Outline each blood parasite and name the species.
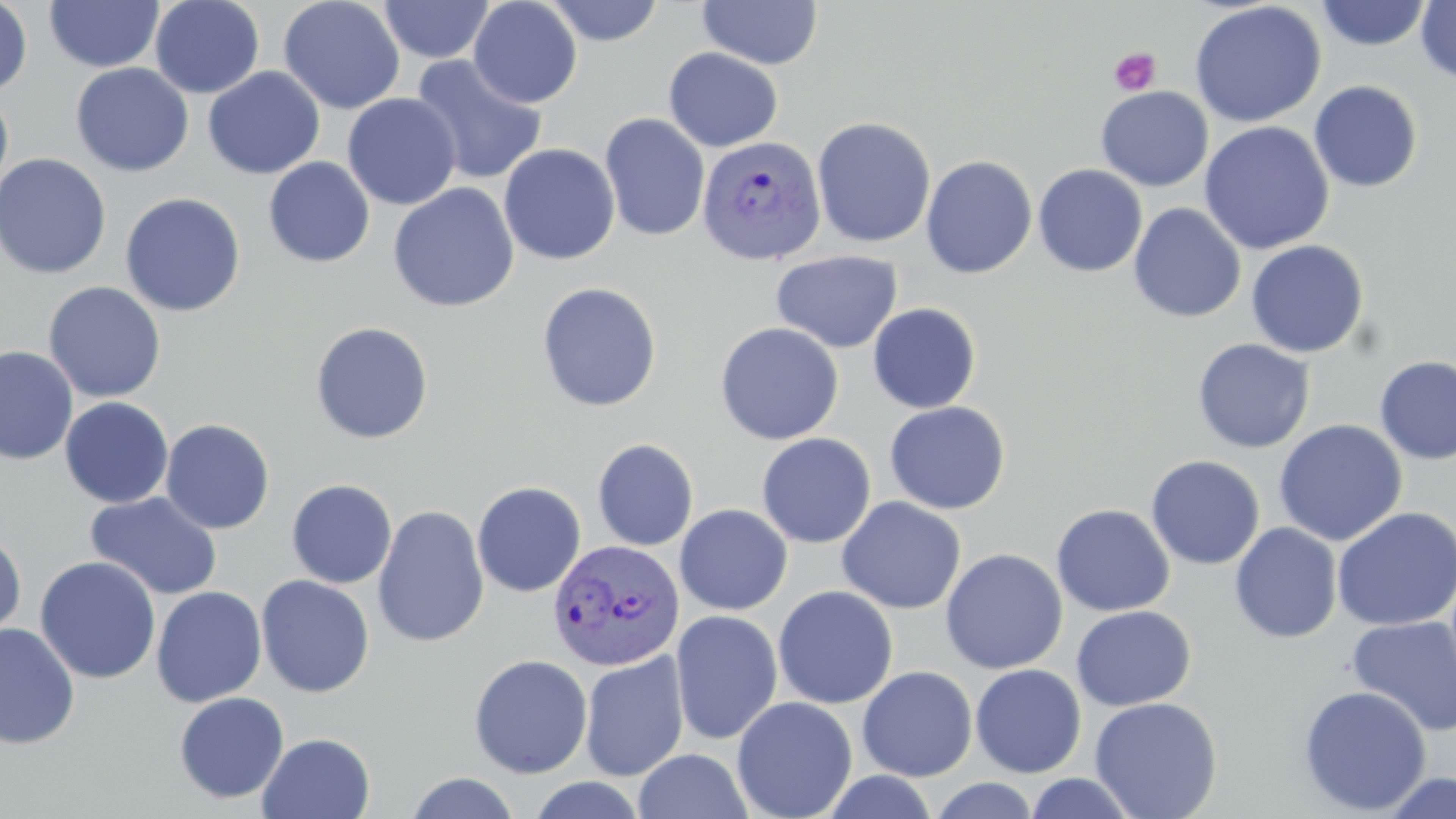
Approximate bounding boxes as (x1, y1, x2, y2) in pixels.
Plasmodium vivax-infected red blood cells: (696, 135, 826, 265), (547, 538, 684, 671).
No Plasmodium falciparum, Plasmodium ovale, Plasmodium malariae, Babesia divergens, or Trypanosoma brucei observed.

slide_level_diagnosis: Plasmodium vivax
magnification: 1000x
uninfected_red_blood_cell_locations: 'approximate bounding boxes as (x1, y1, x2, y2) in pixels: (0, 0, 33, 97), (149, 0, 264, 99), (278, 0, 406, 115), (468, 0, 582, 108), (543, 0, 664, 46), (697, 0, 823, 69), (1376, 0, 1456, 77), (44, 1, 163, 73), (378, 1, 494, 63), (1315, 1, 1432, 51), (1415, 1, 1456, 84), (1189, 2, 1326, 128), (663, 47, 784, 151), (410, 54, 548, 186), (70, 63, 194, 177), (203, 66, 325, 179), (1308, 80, 1423, 193), (1096, 86, 1213, 191), (0, 87, 14, 203), (342, 93, 462, 210), (599, 113, 710, 241), (811, 116, 936, 248), (1199, 121, 1335, 254), (498, 143, 620, 265), (0, 152, 112, 280), (921, 154, 1038, 278), (263, 156, 375, 268), (1033, 164, 1147, 277), (387, 183, 520, 313), (120, 192, 246, 317), (1129, 203, 1246, 323), (1245, 239, 1369, 358), (770, 250, 903, 353), (43, 281, 166, 403), (536, 282, 662, 412), (867, 303, 982, 414), (310, 321, 434, 444), (714, 322, 844, 445), (1192, 338, 1316, 453), (0, 345, 78, 464), (1375, 355, 1456, 466), (59, 396, 174, 508), (884, 401, 1010, 515), (160, 418, 275, 534), (1273, 419, 1408, 546), (756, 432, 876, 548), (592, 439, 698, 551), (1146, 455, 1265, 570), (272, 478, 388, 686), (286, 479, 398, 588), (472, 480, 586, 597), (85, 491, 223, 600), (836, 496, 966, 614), (675, 503, 792, 615), (1051, 503, 1174, 617), (373, 504, 489, 648), (1331, 506, 1456, 630), (1229, 523, 1343, 644), (0, 532, 27, 644), (940, 548, 1067, 674), (34, 556, 161, 684), (255, 574, 375, 697), (150, 586, 267, 707), (772, 586, 898, 708), (1070, 606, 1196, 711), (670, 610, 783, 745), (1346, 615, 1456, 737), (0, 623, 80, 749), (578, 651, 689, 782), (468, 654, 593, 779), (970, 664, 1087, 778), (857, 666, 977, 781), (1297, 685, 1432, 816), (173, 692, 290, 804), (1089, 696, 1223, 818), (732, 697, 858, 818), (257, 732, 375, 819), (633, 749, 753, 818), (819, 770, 939, 818), (1378, 771, 1456, 819), (403, 772, 522, 818), (1023, 772, 1140, 818), (928, 777, 1042, 818)'
stain: May-Grünwald-Giemsa
modality: optical microscopy
preparation: thin blood film
image_size: 1456×819 pixels
field_of_view: single
platelet_locations: 'approximate bounding boxes as (x1, y1, x2, y2) in pixels: (1109, 47, 1162, 96)'